Assess this cell for malaria.
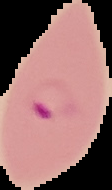
It is parasitized.

preparation = thin blood film
image type = segmented cell region with the area outside set to black
image size = 112×190 pixels